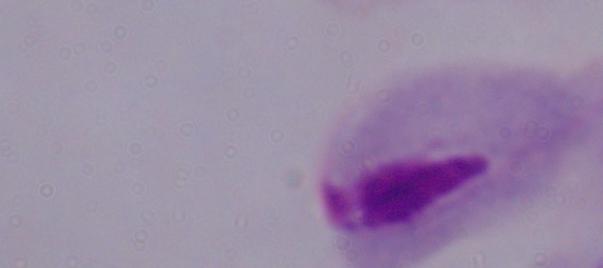
modality: photomicrograph
magnification: 1000x
identification: trichomonad